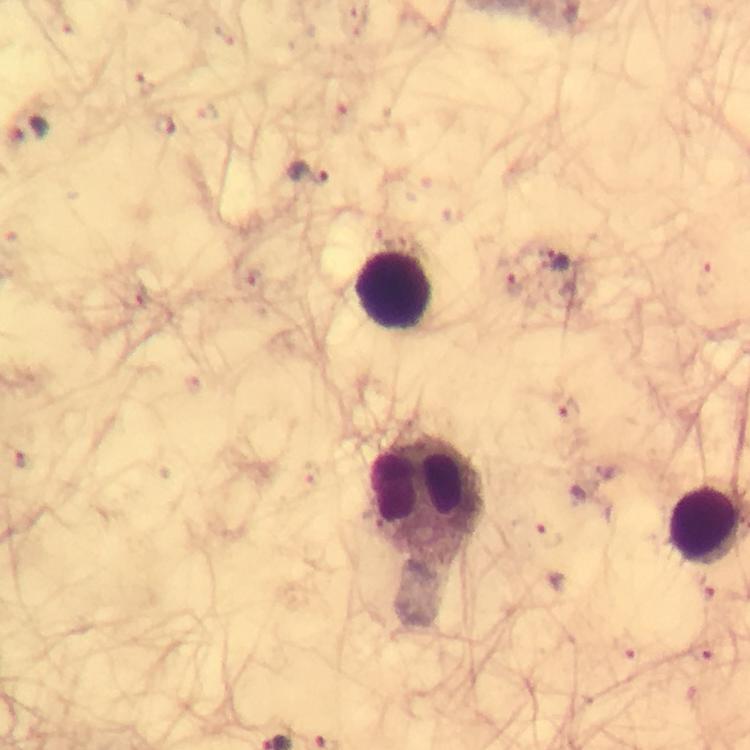
Approximate centers as [x, y] in pixels.
Summary:
  - Plasmodium parasite locations: [144, 83], [165, 123], [29, 131], [306, 171], [556, 261], [253, 283], [514, 285], [131, 300], [568, 410], [545, 535], [704, 590], [623, 647], [701, 652]
  - Leukocyte locations: [395, 290], [424, 497], [706, 527]
  - Magnification: 100x
  - Context: from a diagnostic examination for malaria
  - Immersion oil: applied
  - Image size: 750×750 pixels
  - Cropped from: one field of view
  - Stain: Giemsa
  - Preparation: thick smear
  - Capture: smartphone camera through the microscope